Identify the parasite.
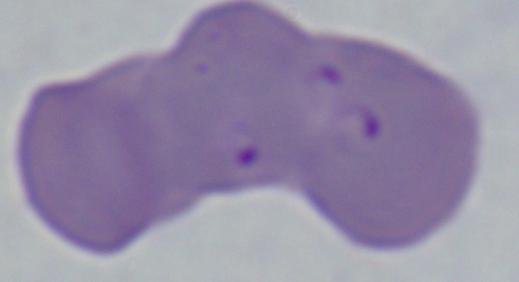
This is Babesia.

1000x magnification. Photomicrograph.